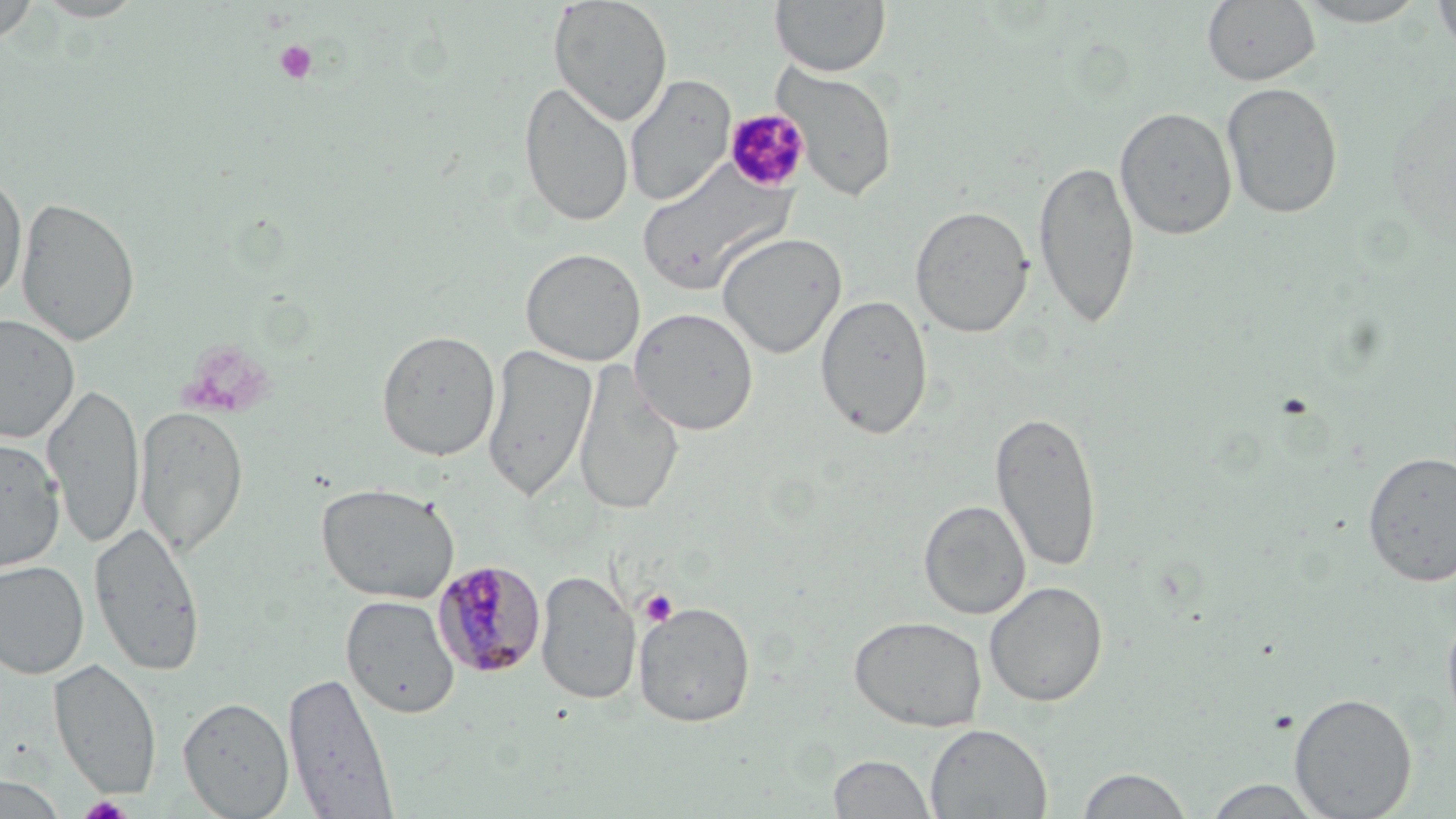
{
  "slide_level_diagnosis": "Plasmodium malariae",
  "modality": "light microscopy",
  "magnification": "1000x",
  "plasmodium_malariae_infected_red_blood_cell_locations": "approximate bounding boxes as [x1, y1, x2, y2] in pixels: [431, 558, 546, 680]",
  "stain": "May-Grünwald-Giemsa",
  "field_of_view": "one of a larger specimen",
  "platelet_locations": "approximate bounding boxes as [x1, y1, x2, y2] in pixels: [274, 40, 318, 85], [726, 105, 809, 194], [639, 589, 678, 627], [79, 795, 133, 818]",
  "preparation": "thin blood film",
  "uninfected_red_blood_cell_locations": "approximate bounding boxes as [x1, y1, x2, y2] in pixels: [548, 0, 673, 126], [770, 0, 891, 77], [1201, 0, 1320, 87], [1292, 0, 1433, 27], [1432, 0, 1456, 57], [0, 2, 40, 45], [770, 62, 899, 203], [624, 74, 736, 206], [518, 80, 634, 227], [1221, 81, 1344, 220], [1114, 106, 1237, 240], [1033, 158, 1140, 329], [636, 160, 795, 296], [0, 170, 28, 304], [16, 196, 141, 347], [910, 204, 1035, 339], [717, 232, 847, 359], [520, 247, 646, 366], [815, 293, 933, 440], [629, 306, 759, 435], [0, 313, 79, 443], [376, 329, 501, 461], [482, 343, 597, 501], [573, 361, 684, 518], [43, 381, 145, 550], [135, 404, 249, 558], [990, 409, 1103, 574], [0, 435, 66, 573], [1362, 451, 1456, 587], [315, 481, 460, 604], [918, 500, 1032, 620], [88, 521, 206, 677], [0, 559, 90, 679], [535, 569, 641, 705], [984, 580, 1108, 707], [341, 595, 460, 719], [634, 601, 756, 727], [1441, 603, 1456, 734], [848, 615, 988, 732], [48, 658, 162, 798], [282, 670, 398, 818], [1289, 692, 1417, 818], [178, 696, 295, 818], [925, 724, 1052, 818], [827, 753, 937, 818], [1075, 767, 1196, 818], [0, 774, 67, 818], [1200, 778, 1328, 818]",
  "image_size": "1456×819 pixels"
}